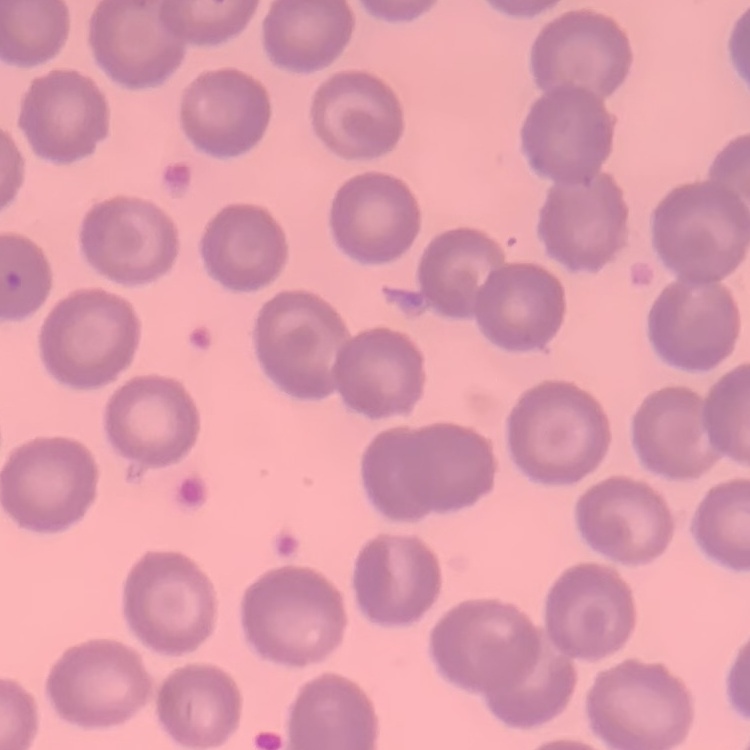

Summary:
  - Red blood cell morphology: no rouleaux formation
  - Image type: one tile cut from a larger photomicrograph
  - Preparation: thin blood smear
  - Stain: Field's or Giemsa